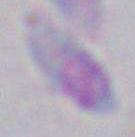

identification = Toxoplasma gondii
modality = photomicrograph
magnification = 1000x